Report the malaria status of this cell.
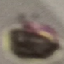
Uninfected.

{
  "preparation": "thin blood smear",
  "capture": "smartphone camera at the microscope eyepiece",
  "stain": "Giemsa",
  "image_type": "cell patch, automatically extracted from a larger field of view and resized to 64 × 64 pixels"
}